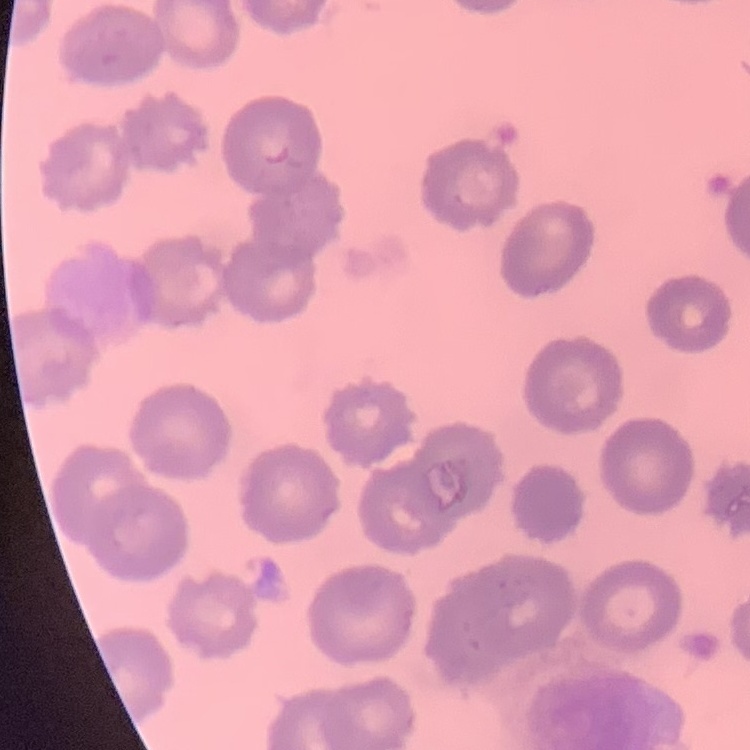
erythrocyte morphology = no rouleaux formation
preparation = thin peripheral smear
image type = one tile cut from a larger photomicrograph
stain = Field's or Giemsa